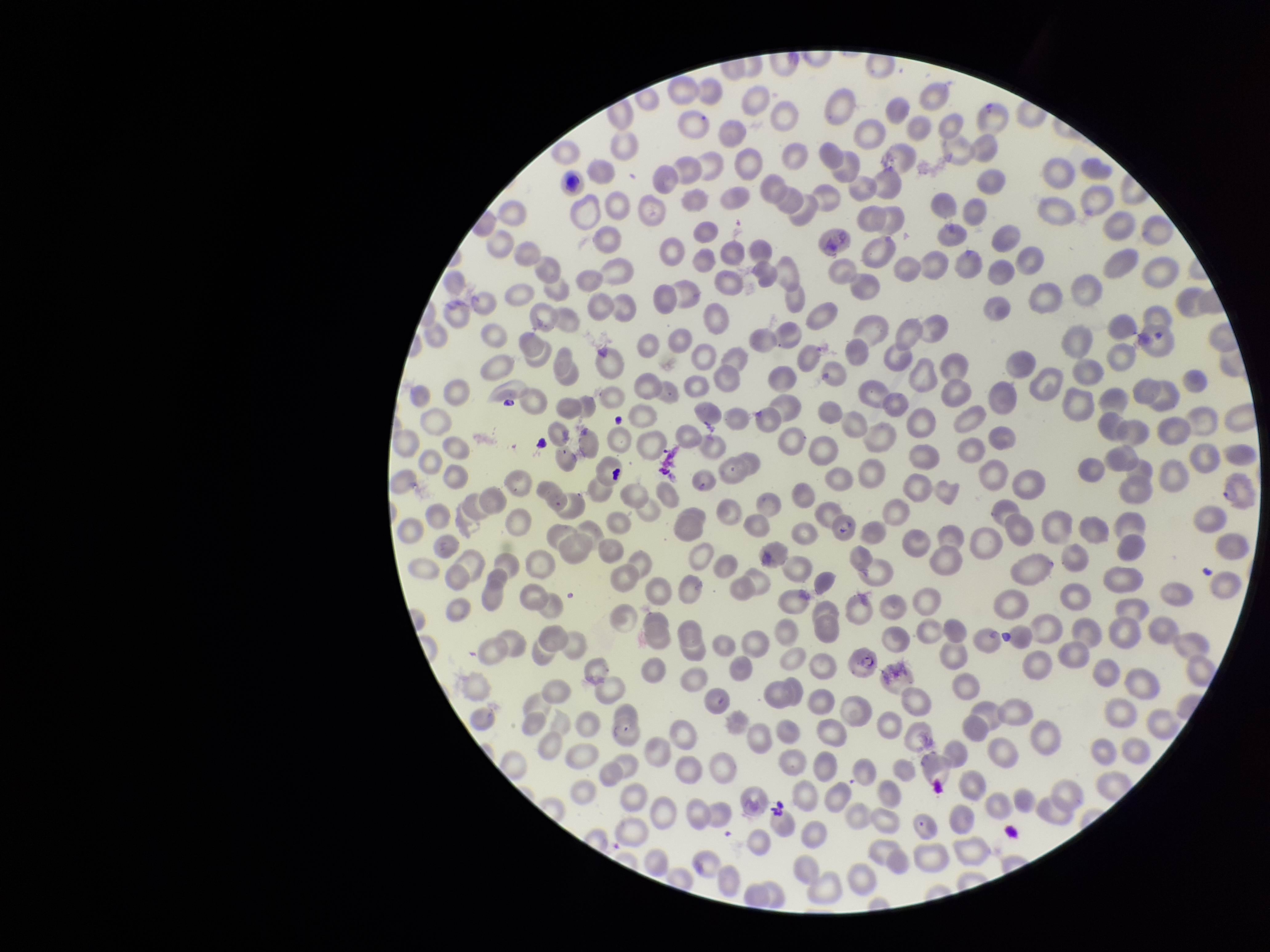
parasitized red blood cells = none identified
parasitized red blood cell count = 0
capture = smartphone photograph through the microscope eyepiece
red blood cell count = 338
species reported for this patient = Plasmodium falciparum
image size = 1270×952 pixels
stain = Giemsa
field of view = single
patient malaria status = infected
preparation = thin